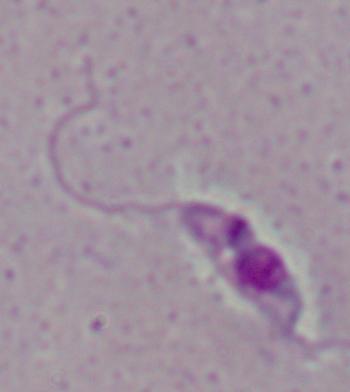

A Leishmania parasite is seen. Captured at 1000x magnification. Photomicrograph.